Outline every parasitised red blood cell.
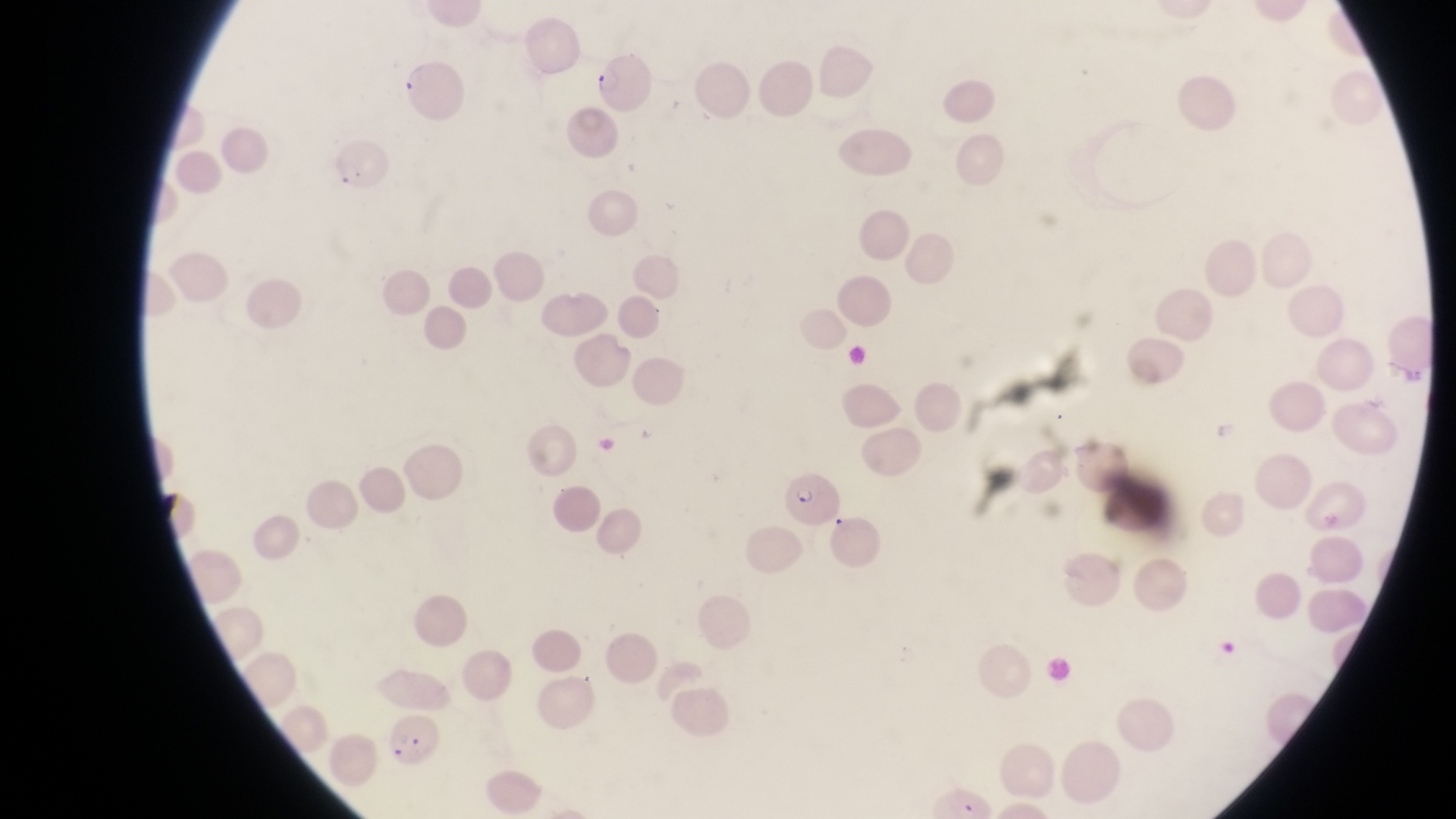

Approximate bounding boxes as {left, top, right, bottom} in pixels.
Parasitised red blood cells: {591, 47, 654, 111}, {394, 55, 467, 128}, {330, 135, 389, 194}, {782, 472, 841, 525}, {380, 711, 441, 769}.

Summary:
  - Trophozoite locations: {1397, 356, 1426, 389}
  - Preparation: thin blood smear
  - Capture: smartphone photograph through the eyepiece of an Olympus CX-23 microscope
  - Field of view: single
  - Country: Uganda
  - Image size: 1456×819 pixels
  - Magnification: 1000x